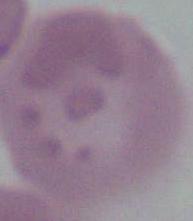

Captured at 1000x magnification. Micrograph. An erythrocyte is shown.